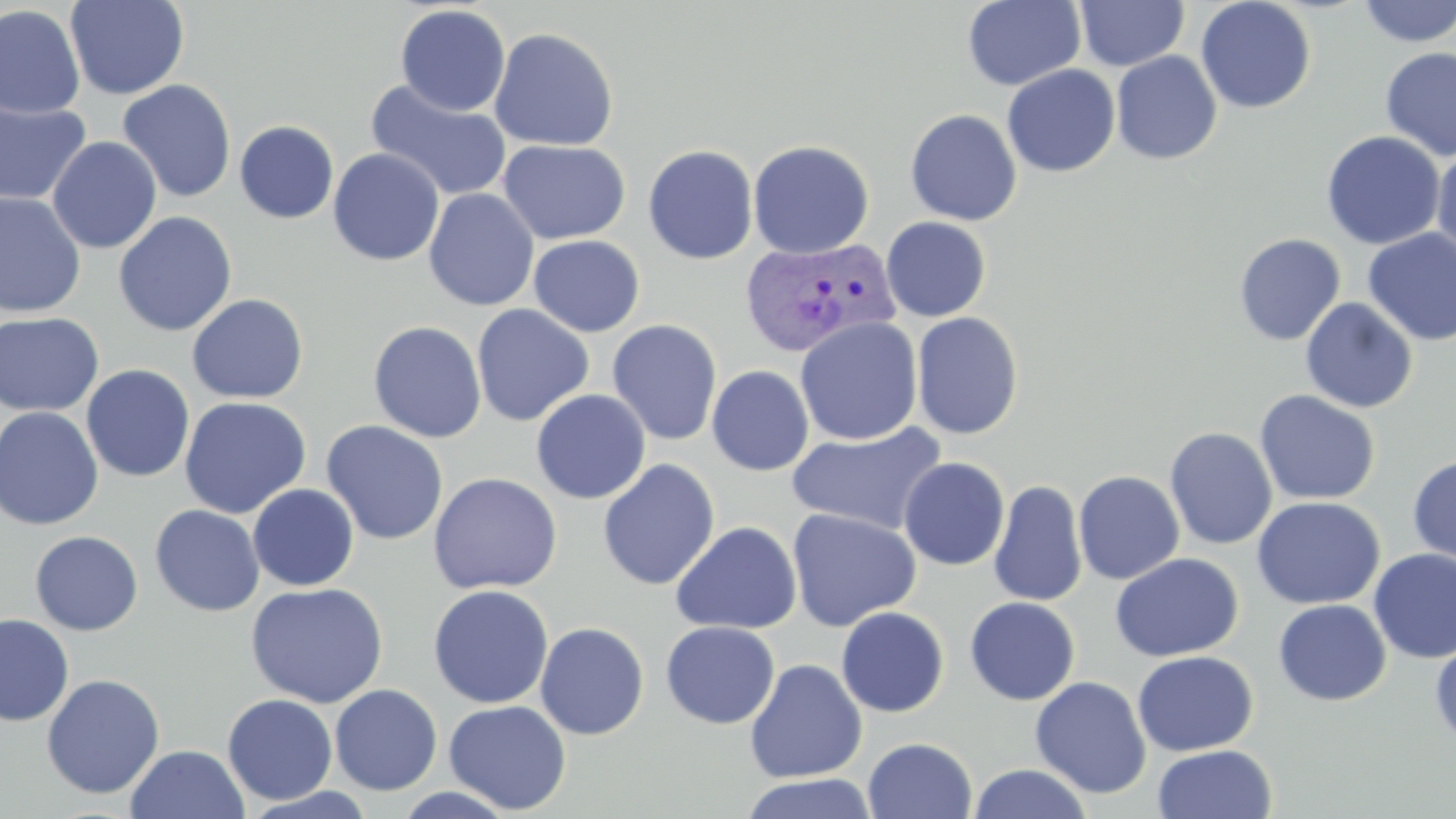

Approximate bounding boxes as (x1, y1, x2, y2) in pixels. Plasmodium vivax-infected red blood cell locations: (739, 236, 899, 359). Uninfected red blood cell locations: (65, 0, 189, 100), (962, 0, 1086, 91), (1195, 0, 1316, 114), (1355, 0, 1456, 48), (1074, 1, 1189, 71), (395, 4, 511, 116), (0, 5, 85, 120), (489, 27, 619, 152), (1379, 46, 1456, 161), (1111, 50, 1222, 165), (1002, 64, 1120, 177), (365, 78, 513, 202), (117, 79, 237, 203), (0, 98, 91, 206), (904, 109, 1022, 226), (234, 121, 339, 224), (1321, 131, 1446, 249), (47, 136, 163, 254), (498, 139, 630, 244), (748, 139, 874, 260), (643, 144, 758, 265), (1432, 146, 1456, 263), (328, 148, 445, 267), (423, 188, 539, 311), (0, 191, 86, 318), (114, 211, 237, 336), (881, 217, 991, 321), (1361, 229, 1456, 345), (1233, 233, 1346, 345), (528, 235, 645, 337), (186, 293, 309, 404), (1300, 297, 1418, 413), (471, 304, 594, 426), (912, 311, 1024, 440), (0, 312, 105, 417), (795, 317, 923, 446), (606, 320, 723, 446), (367, 321, 487, 443), (81, 365, 195, 482), (707, 366, 814, 476), (531, 389, 651, 504), (1254, 390, 1381, 505), (178, 396, 311, 519), (0, 406, 104, 530), (321, 420, 448, 545), (785, 422, 949, 536), (1164, 426, 1277, 550), (1407, 453, 1456, 567), (898, 457, 1009, 571), (597, 459, 720, 591), (1073, 470, 1185, 585), (427, 472, 562, 594), (989, 480, 1087, 607), (248, 484, 360, 591), (1252, 496, 1384, 610), (149, 504, 265, 617), (786, 508, 922, 631), (671, 521, 802, 635), (29, 531, 143, 636), (1369, 548, 1456, 665), (1110, 552, 1244, 662), (246, 582, 388, 708), (427, 585, 554, 708), (964, 596, 1081, 706), (1273, 599, 1391, 706), (836, 606, 949, 717), (0, 615, 74, 726), (660, 621, 780, 729), (535, 622, 649, 740), (1430, 635, 1456, 749), (1132, 650, 1258, 756), (745, 659, 867, 783), (42, 674, 165, 799), (1030, 676, 1152, 798), (330, 684, 443, 795), (222, 693, 338, 805), (443, 700, 572, 814), (863, 737, 977, 819), (125, 744, 250, 819), (1152, 744, 1278, 819), (864, 751, 1091, 818), (967, 764, 1094, 819), (736, 772, 879, 818), (389, 786, 520, 818). Slide-level diagnosis: Plasmodium vivax. Single field of view. Captured at 1000x magnification. May-Grünwald-Giemsa stain. Thin blood smear. Image is 1456×819 pixels. Light microscopy.